Name the blood parasite species.
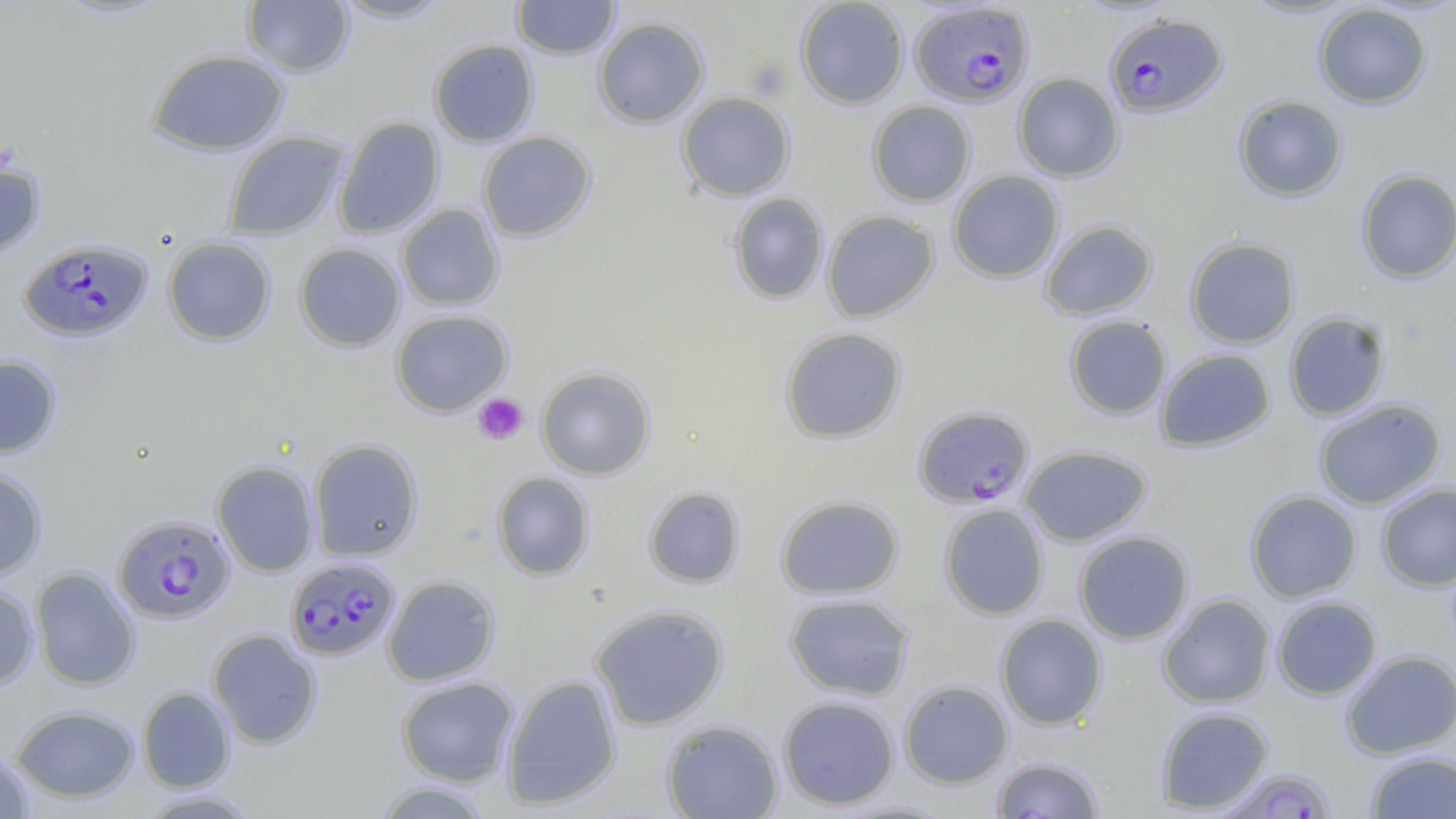

Plasmodium falciparum.

Summary:
  - Coordinate format: approximate bounding boxes as (x1, y1, x2, y2) in pixels
  - Uninfected red blood cell locations: (332, 0, 451, 23), (512, 0, 620, 59), (795, 0, 909, 109), (242, 1, 354, 77), (1314, 3, 1432, 109), (592, 16, 709, 129), (428, 40, 539, 147), (146, 49, 289, 156), (1013, 72, 1124, 181), (676, 92, 795, 201), (1233, 95, 1348, 202), (867, 101, 976, 206), (333, 116, 445, 239), (223, 131, 349, 240), (477, 131, 597, 242), (0, 160, 45, 259), (947, 170, 1064, 283), (1355, 170, 1456, 283), (728, 193, 829, 305), (396, 204, 504, 311), (821, 210, 939, 322), (1039, 219, 1158, 320), (162, 236, 276, 346), (1184, 237, 1301, 349), (294, 243, 406, 352), (390, 310, 513, 416), (1283, 311, 1391, 421), (1064, 315, 1172, 420), (778, 326, 908, 443), (1155, 348, 1275, 452), (0, 355, 61, 458), (536, 366, 656, 480), (1313, 398, 1446, 510), (308, 439, 423, 561), (1019, 445, 1153, 546), (212, 461, 319, 576), (0, 468, 47, 581), (491, 471, 594, 580), (1376, 483, 1456, 591), (643, 485, 746, 588), (1244, 490, 1362, 603), (775, 495, 904, 600), (939, 503, 1050, 620), (1073, 531, 1194, 644), (30, 567, 140, 690), (383, 575, 500, 687), (0, 582, 39, 689), (783, 592, 916, 700), (1157, 594, 1275, 708), (1271, 596, 1382, 699), (589, 603, 729, 730), (995, 614, 1108, 730), (208, 629, 322, 748), (1341, 650, 1456, 759), (501, 675, 621, 810), (396, 676, 518, 786), (899, 680, 1013, 788), (137, 687, 235, 792), (778, 695, 900, 810), (11, 705, 139, 804), (1155, 706, 1274, 813), (661, 719, 782, 819), (0, 750, 34, 818), (1365, 751, 1456, 818), (992, 756, 1105, 818), (370, 780, 495, 818), (138, 790, 262, 818)
  - Plasmodium falciparum-infected red blood cell locations: (910, 1, 1034, 107), (1104, 13, 1228, 116), (20, 239, 152, 341), (914, 405, 1034, 508), (113, 515, 235, 624), (286, 557, 400, 661), (1218, 767, 1338, 818)
  - Platelet locations: (748, 59, 792, 100), (473, 393, 529, 445)
  - Magnification: 1000x
  - Stain: May-Grünwald-Giemsa
  - Field of view: one of a larger specimen
  - Preparation: thin blood smear
  - Modality: light microscopy
  - Image size: 1456×819 pixels